Classify this cell by malaria status.
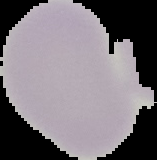
It is uninfected.

image_type: segmented cell region on a black background
preparation: thin blood film
image_size: 157×160 pixels